Identify the blood parasite species.
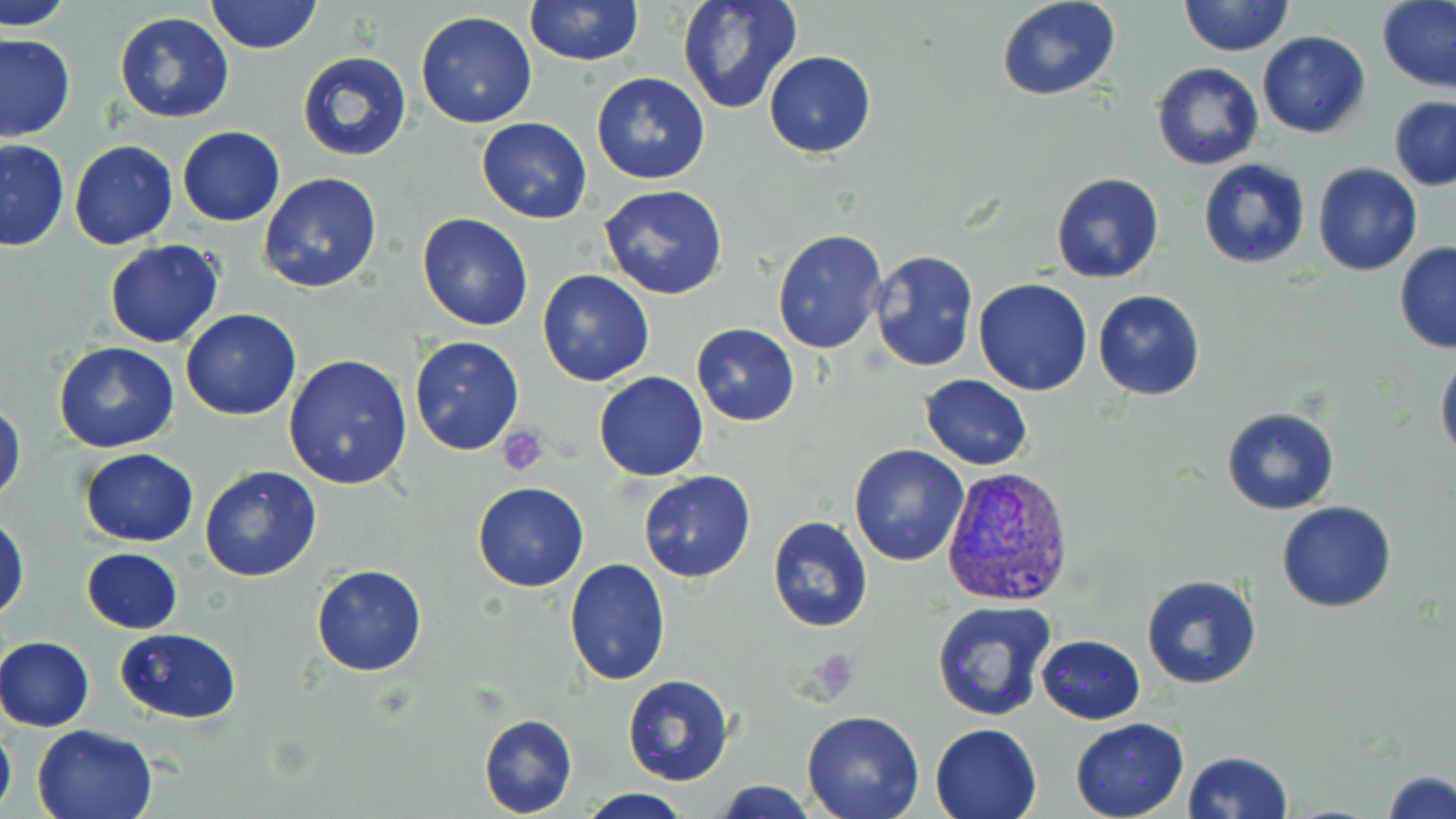
Plasmodium vivax.

Summary:
  - Coordinate format: approximate bounding boxes as (x1,y1)-(x2,y2) corner pairs in pixels
  - Plasmodium vivax-infected red blood cell locations: (940,463)-(1076,606)
  - Platelet locations: (499,426)-(549,476), (807,649)-(863,700)
  - Uninfected red blood cell locations: (4,0)-(75,31), (204,0)-(323,55), (524,0)-(644,66), (677,0)-(803,114), (997,0)-(1120,100), (1179,0)-(1293,56), (1378,0)-(1456,92), (415,11)-(538,128), (115,12)-(235,123), (1257,30)-(1371,140), (0,32)-(75,141), (764,50)-(876,159), (297,51)-(411,162), (1153,62)-(1263,170), (590,73)-(711,186), (1388,97)-(1456,191), (476,117)-(592,224), (177,127)-(285,226), (69,139)-(178,250), (0,140)-(70,253), (1197,159)-(1311,269), (1312,163)-(1424,276), (1051,172)-(1164,285), (260,173)-(382,294), (599,185)-(729,299), (417,212)-(533,330), (771,229)-(887,353), (103,240)-(225,348), (1394,242)-(1456,353), (867,249)-(979,374), (538,269)-(654,386), (972,278)-(1093,397), (1093,289)-(1206,400), (181,309)-(302,421), (691,322)-(800,426), (409,337)-(525,455), (53,342)-(179,452), (284,352)-(414,490), (1436,353)-(1456,466), (594,372)-(708,482), (919,375)-(1034,470), (0,400)-(26,504), (1222,407)-(1338,514), (848,443)-(970,566), (80,448)-(199,546), (199,464)-(322,581), (638,469)-(756,583), (472,482)-(589,593), (1277,501)-(1397,614), (1,513)-(29,622), (767,516)-(873,633), (82,547)-(183,633), (563,557)-(671,687), (311,565)-(427,676), (1141,573)-(1264,690), (931,598)-(1058,723), (113,627)-(242,725), (1037,634)-(1144,724), (0,636)-(94,732), (622,675)-(735,787), (801,709)-(925,819), (478,714)-(578,817), (0,718)-(16,818), (1069,718)-(1190,819), (31,722)-(158,819), (930,722)-(1043,819), (1181,751)-(1294,819), (1383,771)-(1456,819), (707,779)-(821,818), (574,790)-(697,819)
  - Field of view: one of a larger specimen
  - Preparation: thin blood film
  - Stain: May-Grünwald-Giemsa
  - Image size: 1456×819 pixels
  - Modality: optical microscopy
  - Magnification: 1000x